Report the malaria status of this cell.
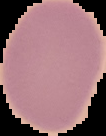

Uninfected.

Image is 106×136 pixels. From a thin blood smear. Segmented cell region on a black background.